Assess the morphology of the red blood cells.
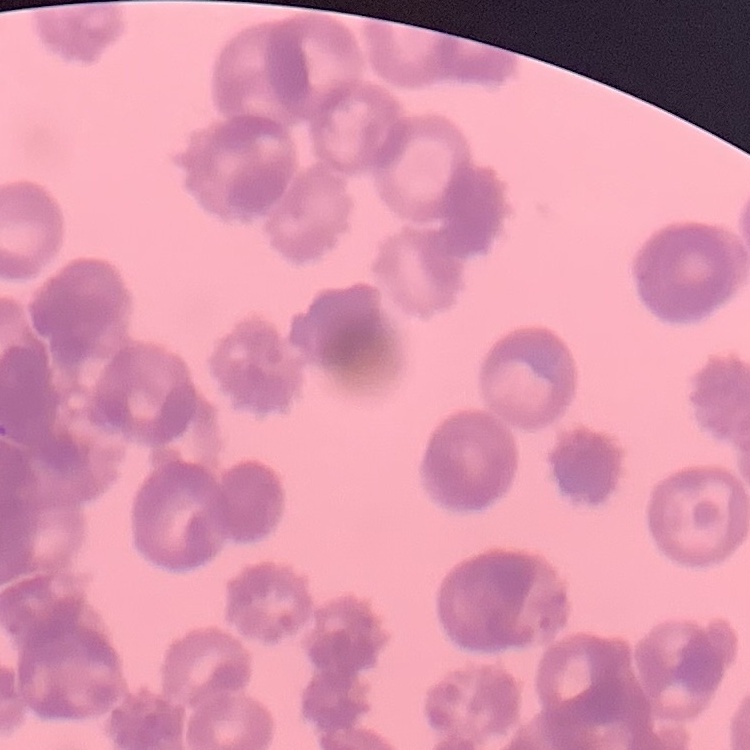
They show rouleaux formation.

preparation = thin blood smear
stain = Field's or Giemsa
image type = square crop of a larger photomicrograph